Classify this cell by malaria status.
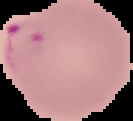
It is parasitized.

Cell region segmented out of the field of view; the surrounding area is masked to black. Image is 133×121 pixels. From a thin blood smear.